Assess the morphology of the red blood cells.
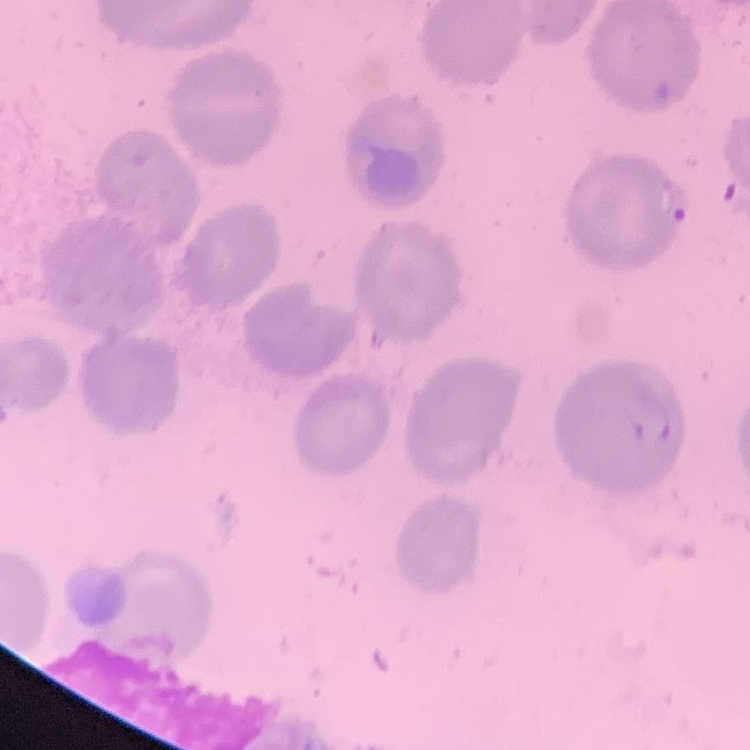
They show no rouleaux formation.

stain: Field's or Giemsa
image_type: one tile cut from a larger photomicrograph
preparation: thin blood smear